Assess this cell for malaria.
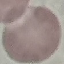
It is uninfected.

Summary:
  - Preparation: thin smear
  - Capture: smartphone through the microscope eyepiece
  - Image type: automatically extracted cell patch, resized to 64 × 64 pixels
  - Stain: Giemsa